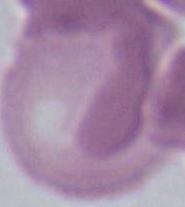
{
  "identification": "erythrocyte",
  "modality": "photomicrograph",
  "magnification": "1000x"
}